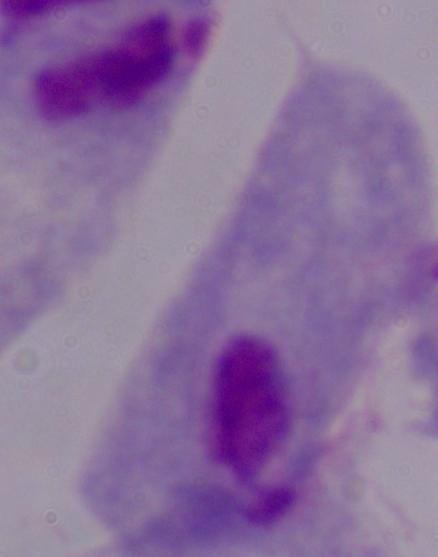
magnification = 1000x
modality = photomicrograph
identification = trichomonad